Outline each Trypanosoma brucei.
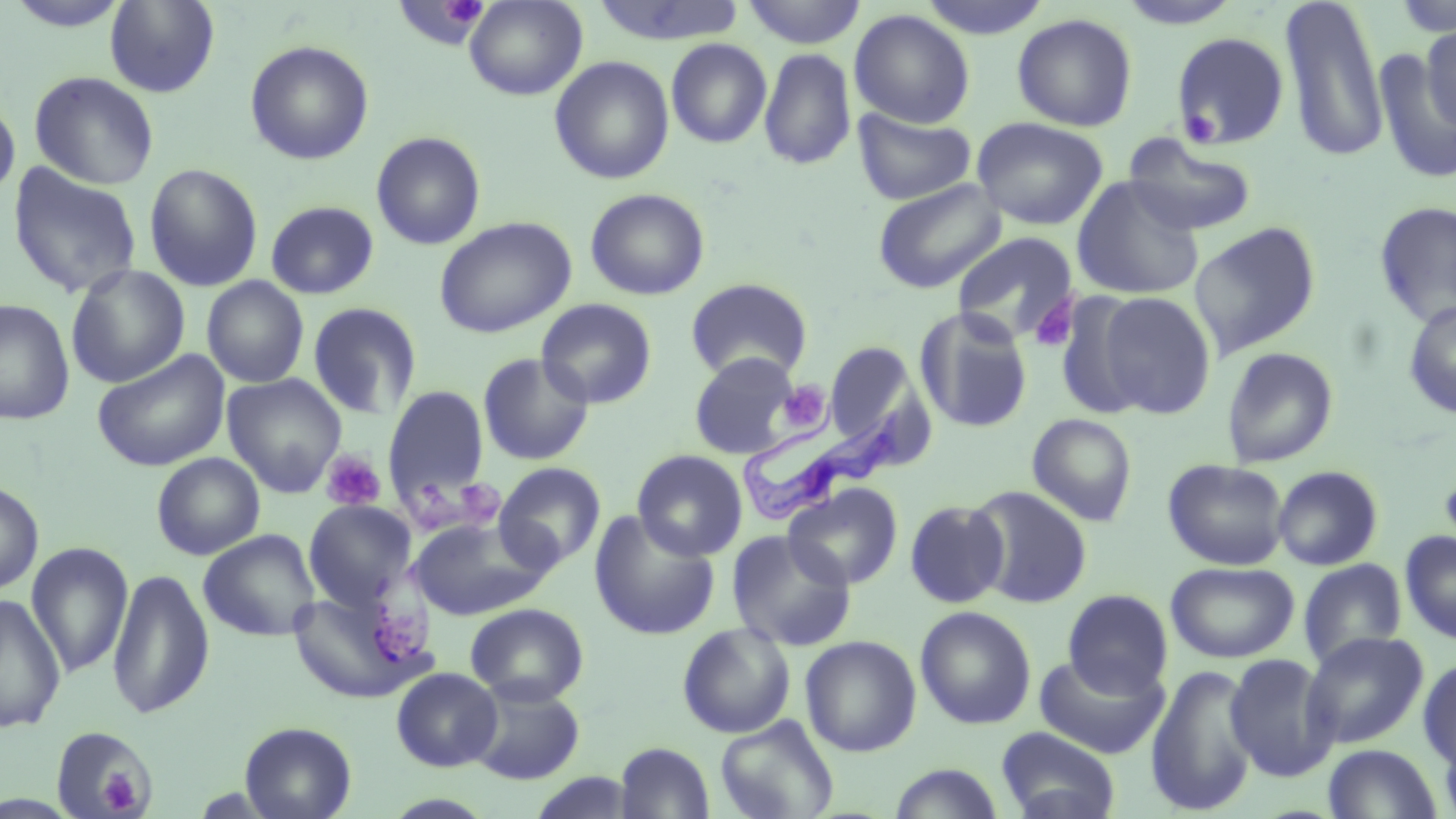

Approximate bounding boxes as (x1,y1)-(x2,y2) corner pairs in pixels.
Trypanosoma brucei: (734,417)-(900,525).

slide-level diagnosis = Trypanosoma brucei
magnification = 1000x
image size = 1456×819 pixels
uninfected red blood cell locations = approximate bounding boxes as (x1,y1)-(x2,y2) corner pairs in pixels: (392,0)-(488,48), (464,0)-(587,100), (590,0)-(748,46), (741,0)-(867,49), (915,0)-(1054,39), (1115,0)-(1247,30), (1391,0)-(1456,39), (104,1)-(220,97), (1279,1)-(1389,165), (849,9)-(975,129), (1012,13)-(1138,132), (1419,25)-(1455,136), (1171,32)-(1290,149), (666,38)-(772,149), (244,40)-(374,165), (758,47)-(856,172), (1373,47)-(1456,186), (549,56)-(675,185), (28,71)-(159,190), (0,99)-(20,199), (852,108)-(977,205), (971,116)-(1108,231), (371,131)-(486,250), (1122,134)-(1258,236), (7,163)-(143,299), (143,163)-(263,292), (1071,177)-(1205,300), (871,178)-(1006,294), (585,188)-(710,301), (265,200)-(379,300), (1373,201)-(1456,328), (434,216)-(576,339), (1188,223)-(1320,359), (951,231)-(1079,345), (66,265)-(189,388), (202,275)-(309,389), (685,277)-(812,382), (1095,290)-(1216,419), (1053,292)-(1158,418), (0,298)-(75,425), (536,298)-(657,409), (1402,300)-(1456,419), (307,301)-(423,419), (914,308)-(1034,434), (824,342)-(917,447), (1221,346)-(1339,468), (92,349)-(230,471), (477,352)-(594,466), (688,352)-(803,459), (222,373)-(346,498), (384,386)-(491,505), (1027,413)-(1137,526), (632,450)-(748,561), (151,452)-(265,560), (1163,459)-(1289,570), (494,462)-(605,572), (1271,465)-(1383,570), (0,480)-(43,595), (783,483)-(903,590), (968,486)-(1093,608), (303,500)-(418,611), (905,500)-(1009,608), (589,511)-(721,641), (409,516)-(554,621), (199,529)-(321,642), (726,530)-(856,652), (1400,530)-(1456,644), (26,542)-(134,679), (1298,558)-(1407,669), (1165,561)-(1299,663), (107,566)-(214,721), (289,586)-(433,705), (1062,589)-(1173,698), (0,594)-(66,733), (465,602)-(589,706), (915,606)-(1037,730), (677,622)-(796,739), (1302,631)-(1429,749), (800,635)-(922,757), (1033,651)-(1169,760), (1224,653)-(1339,782), (1418,658)-(1456,768), (1145,663)-(1260,816), (391,668)-(503,772), (465,680)-(586,785), (715,715)-(839,819), (239,721)-(357,819), (51,725)-(158,819), (996,727)-(1120,819), (1437,728)-(1456,818), (615,742)-(715,819), (1322,743)-(1443,818), (886,763)-(1006,819)
platelet locations = approximate bounding boxes as (x1,y1)-(x2,y2) corner pairs in pixels: (442,1)-(487,28), (1184,109)-(1217,141), (1030,297)-(1077,352), (778,380)-(832,434), (321,450)-(385,512), (453,478)-(502,527), (405,485)-(453,532), (377,608)-(431,667), (99,767)-(142,813)
modality = optical microscopy
field of view = one of a larger specimen
stain = May-Grünwald-Giemsa
preparation = thin blood smear